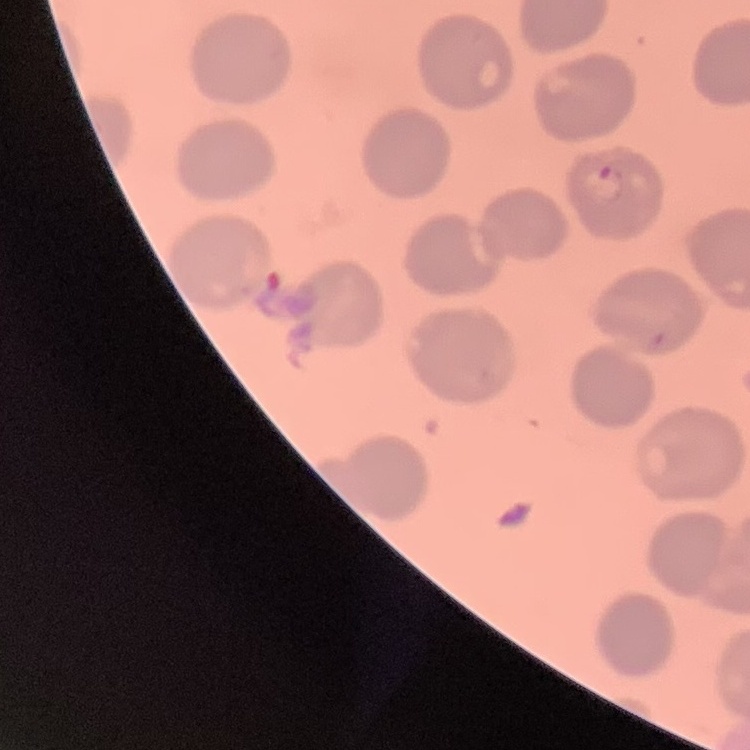
Summary:
  - Red blood cell morphology: no rouleaux formation
  - Image type: square crop of a larger photomicrograph
  - Preparation: thin blood smear
  - Stain: Field's or Giemsa